Give a bounding box for every malaria parasite.
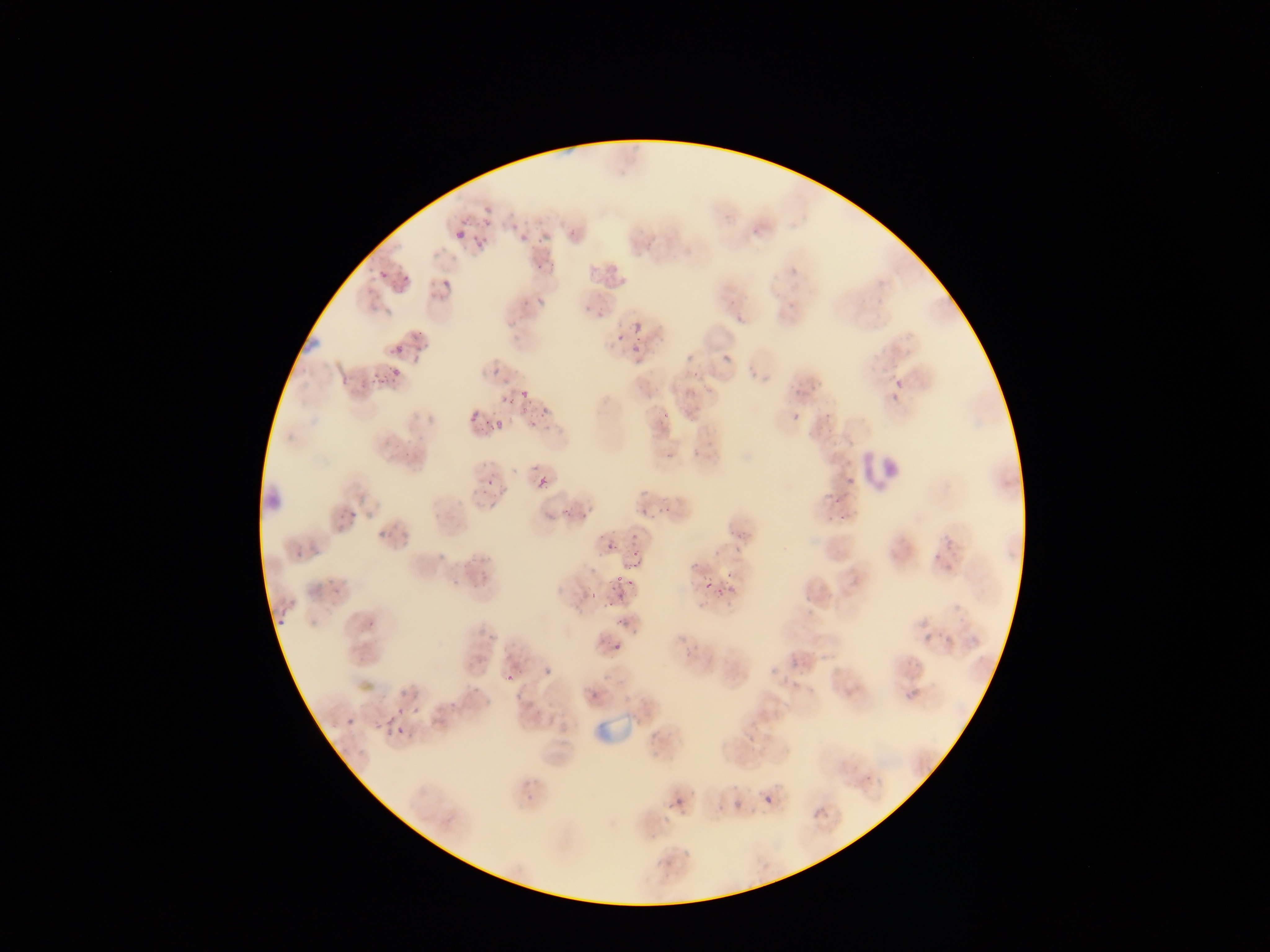
Approximate bounding boxes as [left, top, right, bottom] in pixels.
Malaria parasites: [477, 202, 495, 225], [538, 223, 553, 247], [452, 224, 471, 243], [513, 224, 533, 250], [469, 230, 490, 259], [787, 258, 805, 276], [379, 270, 390, 282], [399, 275, 410, 289], [436, 275, 451, 297], [530, 288, 553, 309], [591, 289, 607, 318], [872, 295, 886, 313], [732, 307, 744, 326], [634, 321, 645, 334], [614, 333, 625, 344], [406, 334, 427, 361], [681, 334, 698, 371], [630, 337, 644, 365], [721, 338, 735, 364], [392, 343, 405, 356], [488, 361, 505, 378], [365, 364, 384, 390], [891, 368, 901, 394], [514, 381, 528, 395], [527, 393, 549, 416], [501, 396, 513, 407], [787, 405, 810, 425], [469, 412, 481, 425], [652, 414, 674, 432], [492, 419, 505, 433], [482, 452, 503, 493], [536, 476, 550, 491], [841, 476, 854, 487], [822, 494, 836, 512], [835, 501, 851, 524], [637, 505, 652, 523], [335, 508, 358, 529], [624, 527, 640, 546], [598, 535, 616, 554], [295, 542, 318, 563], [927, 547, 950, 568], [628, 554, 644, 569], [609, 570, 627, 592], [697, 571, 716, 592], [717, 578, 738, 603], [596, 594, 614, 612], [266, 610, 291, 632], [613, 610, 634, 624], [608, 638, 624, 656], [788, 644, 802, 668], [394, 700, 401, 715], [405, 703, 423, 721], [345, 717, 356, 728], [384, 732, 406, 741], [758, 775, 776, 808], [664, 794, 692, 812].

leukocyte locations = approximate bounding boxes as [left, top, right, bottom] in pixels: [861, 439, 900, 500]
field of view = single
preparation = thin blood smear
image size = 1270×952 pixels
artifact (stain precipitate or debris) locations = approximate bounding boxes as [left, top, right, bottom] in pixels: [259, 478, 287, 513]
capture = mobile-phone photograph through a microscope
country = Ghana